Report the malaria status of this cell.
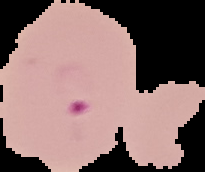
It is parasitized.

From a thin blood smear. Image is 205×172 pixels. Cell region segmented out of the field of view; the surrounding area is masked to black.